Mark where cells are.
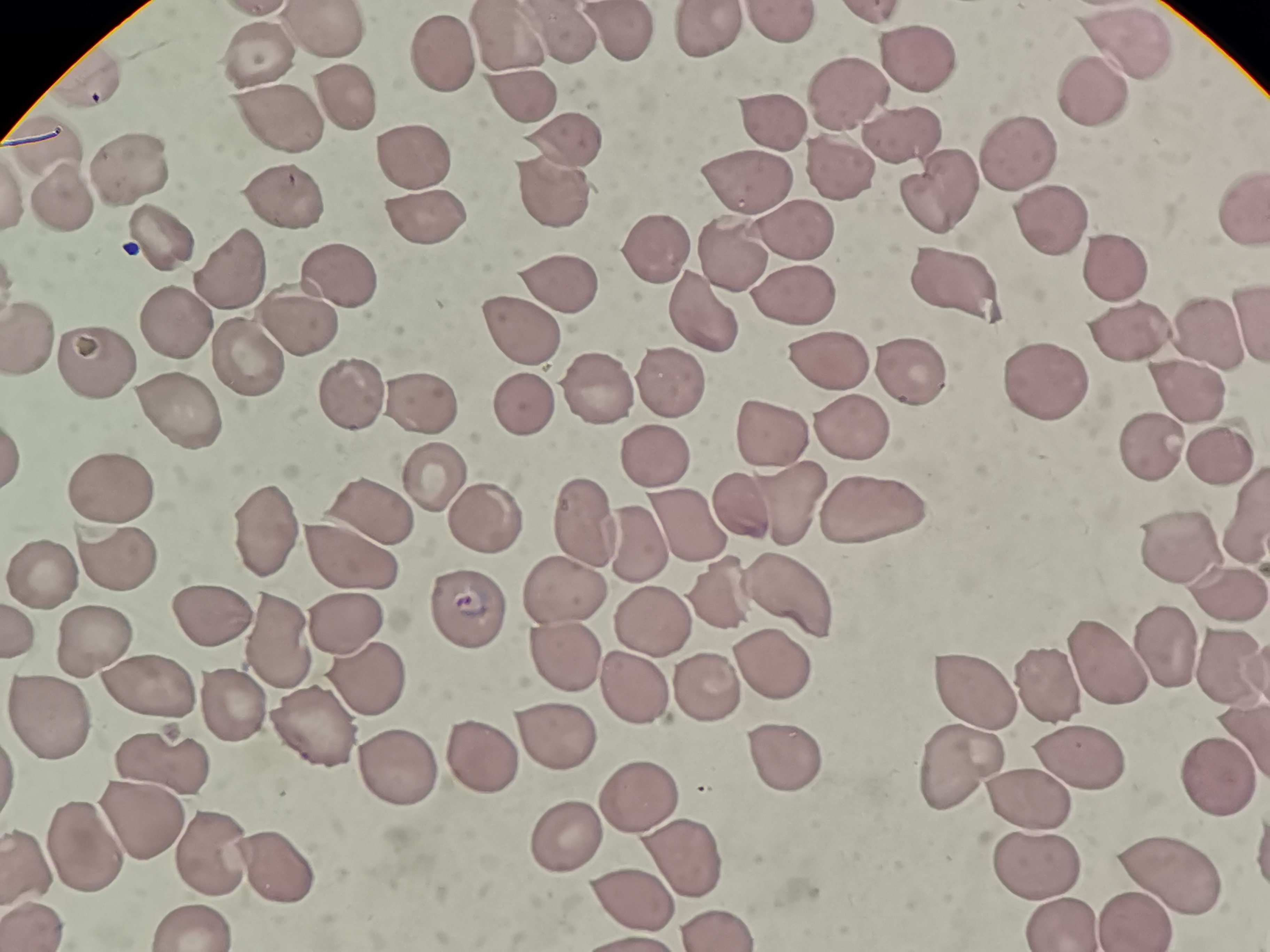
Approximate object centers, in pixels from the top-left corner.
Cells: (x=781, y=23), (x=703, y=28), (x=558, y=35), (x=328, y=39), (x=616, y=40), (x=509, y=45), (x=1122, y=48), (x=916, y=54), (x=261, y=57), (x=448, y=57), (x=849, y=85), (x=1084, y=99), (x=342, y=100), (x=522, y=110), (x=279, y=114), (x=774, y=122), (x=903, y=134), (x=566, y=141), (x=46, y=143), (x=1023, y=149), (x=412, y=161), (x=834, y=167), (x=130, y=175), (x=756, y=180), (x=938, y=187), (x=282, y=192), (x=549, y=195), (x=1242, y=200), (x=63, y=202), (x=1038, y=211), (x=421, y=217), (x=799, y=225), (x=169, y=231), (x=651, y=248), (x=731, y=256), (x=1108, y=260), (x=945, y=279), (x=234, y=280), (x=336, y=288), (x=556, y=289), (x=795, y=297), (x=694, y=309), (x=179, y=319), (x=295, y=326), (x=1127, y=326), (x=521, y=332), (x=1205, y=332), (x=32, y=334), (x=95, y=355), (x=248, y=356), (x=826, y=358), (x=902, y=371), (x=1050, y=379), (x=671, y=380), (x=601, y=387), (x=1183, y=387), (x=348, y=402), (x=424, y=404), (x=173, y=406), (x=848, y=424), (x=771, y=436), (x=1150, y=443), (x=662, y=450), (x=1220, y=452), (x=440, y=481), (x=111, y=494), (x=787, y=502), (x=871, y=506), (x=737, y=513), (x=373, y=516), (x=679, y=517), (x=587, y=518), (x=483, y=522), (x=262, y=525), (x=640, y=542), (x=1167, y=547), (x=113, y=555), (x=341, y=555), (x=46, y=576), (x=1219, y=583), (x=793, y=584), (x=720, y=593), (x=565, y=595), (x=205, y=611), (x=466, y=617), (x=343, y=620), (x=664, y=627), (x=93, y=634), (x=1161, y=641), (x=278, y=648), (x=569, y=659), (x=1227, y=662), (x=765, y=663), (x=1110, y=667), (x=367, y=679), (x=983, y=682), (x=1057, y=684), (x=144, y=685), (x=726, y=689), (x=629, y=691), (x=232, y=710), (x=47, y=714), (x=316, y=731), (x=556, y=740), (x=787, y=753), (x=489, y=756), (x=959, y=756), (x=1068, y=759), (x=159, y=762), (x=399, y=770), (x=1211, y=781), (x=1020, y=791), (x=645, y=794), (x=137, y=819), (x=559, y=836), (x=87, y=848), (x=207, y=852), (x=31, y=855), (x=1039, y=855), (x=682, y=860), (x=275, y=869), (x=1175, y=880), (x=627, y=895), (x=1129, y=915), (x=39, y=918), (x=1054, y=920), (x=186, y=924).

field_of_view: single
capture: smartphone camera at the microscope eyepiece
stain: Giemsa
preparation: thin smear
image_size: 1270×952 pixels